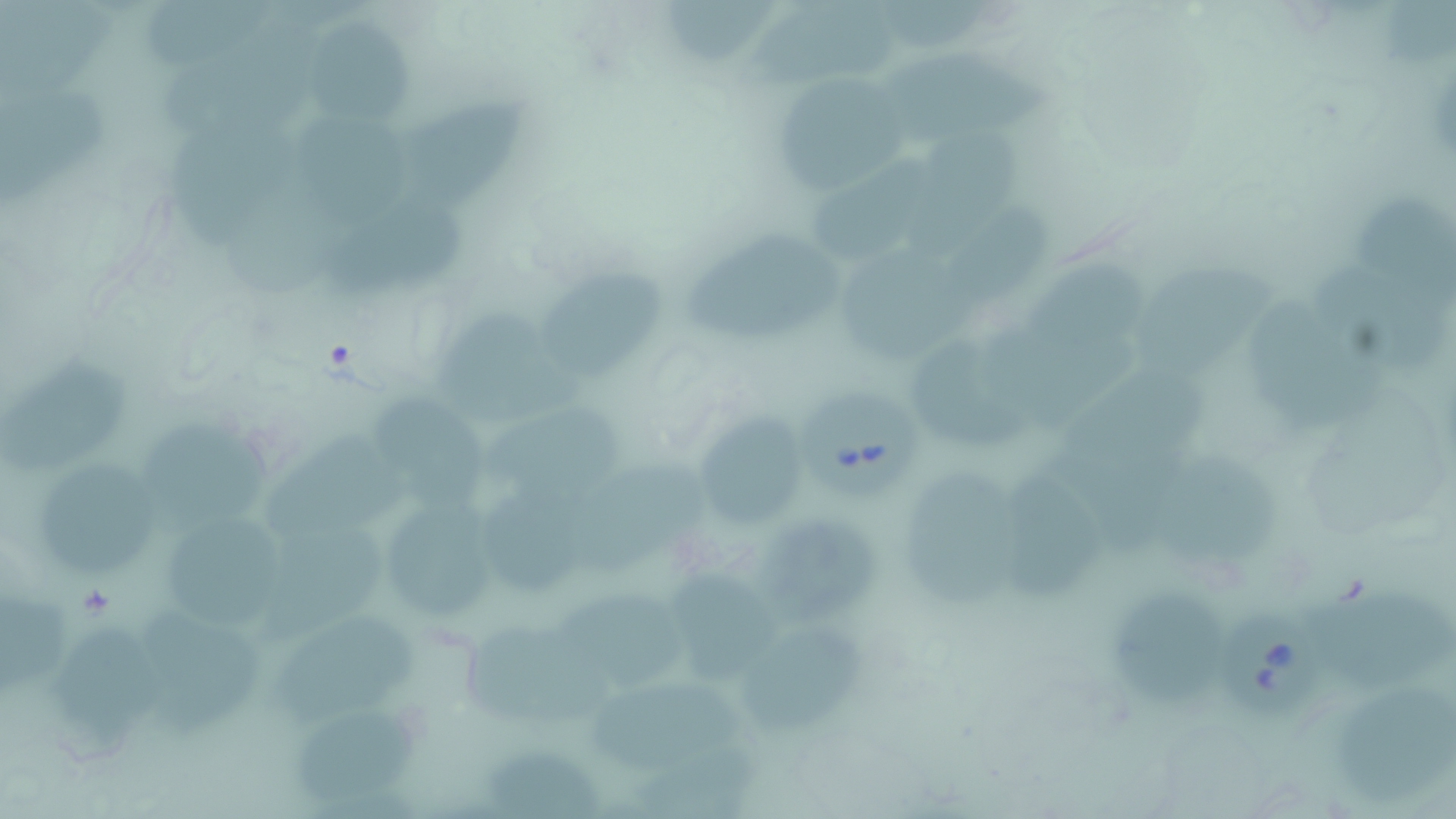

slide_level_diagnosis: Babesia divergens
field_of_view: one of a larger specimen
stain: May-Grünwald-Giemsa
babesia_divergens_infected_red_blood_cell_locations: 'approximate bounding boxes as (x1,y1)-(x2,y2) corner pairs in pixels: (799,389)-(919,500), (1214,604)-(1322,714)'
preparation: thin blood smear
magnification: 1000x
modality: optical microscopy
uninfected_red_blood_cell_locations: 'approximate bounding boxes as (x1,y1)-(x2,y2) corner pairs in pixels: (150,0)-(266,69), (660,0)-(781,66), (760,4)-(904,90), (292,17)-(414,129), (166,20)-(320,137), (883,48)-(1050,147), (771,76)-(911,188), (0,83)-(106,211), (405,96)-(533,208), (174,110)-(303,240), (294,111)-(404,230), (910,131)-(1034,271), (229,150)-(351,293), (815,156)-(939,261), (1359,194)-(1455,295), (943,202)-(1052,304), (334,206)-(475,295), (680,227)-(847,343), (840,252)-(983,357), (1022,257)-(1153,354), (1306,260)-(1449,369), (539,263)-(666,385), (1140,263)-(1278,382), (1251,300)-(1388,433), (440,316)-(585,432), (999,320)-(1135,432), (921,342)-(1035,453), (3,354)-(133,484), (368,389)-(491,521), (491,401)-(629,499), (690,410)-(815,526), (142,415)-(271,529), (269,438)-(421,547), (1152,451)-(1288,569), (41,460)-(156,581), (571,460)-(711,578), (900,462)-(1023,611), (1005,468)-(1103,600), (491,495)-(601,597), (391,502)-(494,621), (165,508)-(292,632), (757,510)-(884,626), (276,519)-(389,633), (674,571)-(778,685), (1320,588)-(1456,687), (1114,590)-(1225,713), (554,591)-(704,699), (268,611)-(429,724), (48,616)-(175,745), (737,621)-(863,735), (466,623)-(618,727), (587,678)-(747,778), (1337,690)-(1456,799), (284,709)-(419,801), (480,748)-(603,819)'
image_size: 1456×819 pixels